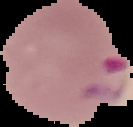
{
  "result": "malaria parasites detected",
  "image_type": "segmented cell region with the area outside set to black",
  "image_size": "133×127 pixels",
  "preparation": "thin blood smear"
}